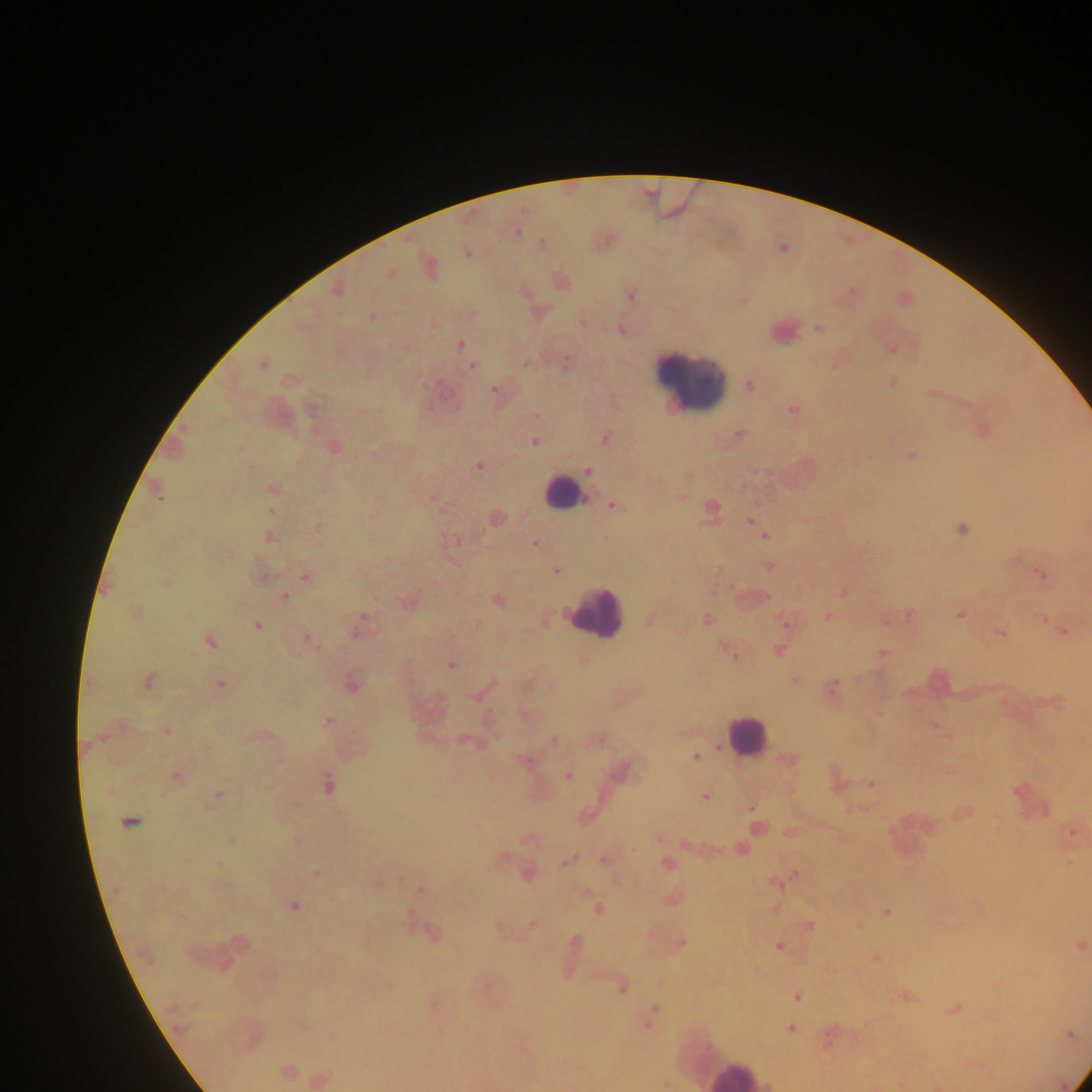

Approximate centers as (x, y) in pixels. Plasmodium parasite locations: (517, 232), (542, 241), (467, 253), (390, 273), (336, 291), (631, 295), (372, 317), (818, 328), (460, 345), (525, 363), (262, 364), (566, 364), (472, 367), (893, 382), (749, 385), (493, 389), (793, 410), (738, 433), (606, 438), (535, 442), (334, 446), (911, 456), (479, 466), (588, 470), (273, 489), (157, 492), (682, 498), (613, 506), (271, 511), (496, 518), (750, 520), (318, 526), (962, 529), (268, 537), (765, 537), (535, 544), (769, 566), (557, 571), (718, 572), (1042, 575), (306, 577), (166, 582), (844, 592), (284, 596), (498, 601), (136, 612), (960, 615), (829, 616), (707, 619), (651, 620), (1044, 620), (888, 621), (785, 622), (257, 626), (476, 626), (356, 630), (1001, 634), (306, 637), (210, 641), (778, 650), (882, 654), (733, 655), (450, 665), (147, 680), (795, 681), (221, 684), (494, 684), (834, 684), (351, 685), (327, 721), (933, 725), (167, 730), (465, 740), (553, 740), (598, 741), (695, 757), (790, 759), (525, 760), (568, 776), (176, 778), (871, 784), (328, 785), (218, 794), (705, 798), (751, 808), (129, 822), (758, 827), (1073, 834), (659, 839), (232, 841), (740, 849), (567, 861), (604, 861), (667, 864), (316, 873), (528, 874), (794, 875), (420, 890), (115, 891), (671, 900), (294, 907), (598, 909), (886, 912), (532, 924), (810, 926), (499, 927), (434, 932), (575, 940), (682, 943), (1081, 945), (779, 946), (877, 957), (622, 989), (797, 997), (907, 997), (433, 1005), (955, 1009), (653, 1011), (792, 1029), (1071, 1035), (332, 1036), (287, 1071). Leukocyte locations: (690, 381), (562, 493), (597, 613), (744, 735), (736, 1074). Thick blood film. Photographed through a microscope with a mobile-phone camera. Image is 1092×1092 pixels. Single field of view. Collected in Ghana.